Give the extent of all uninfected red blood cells.
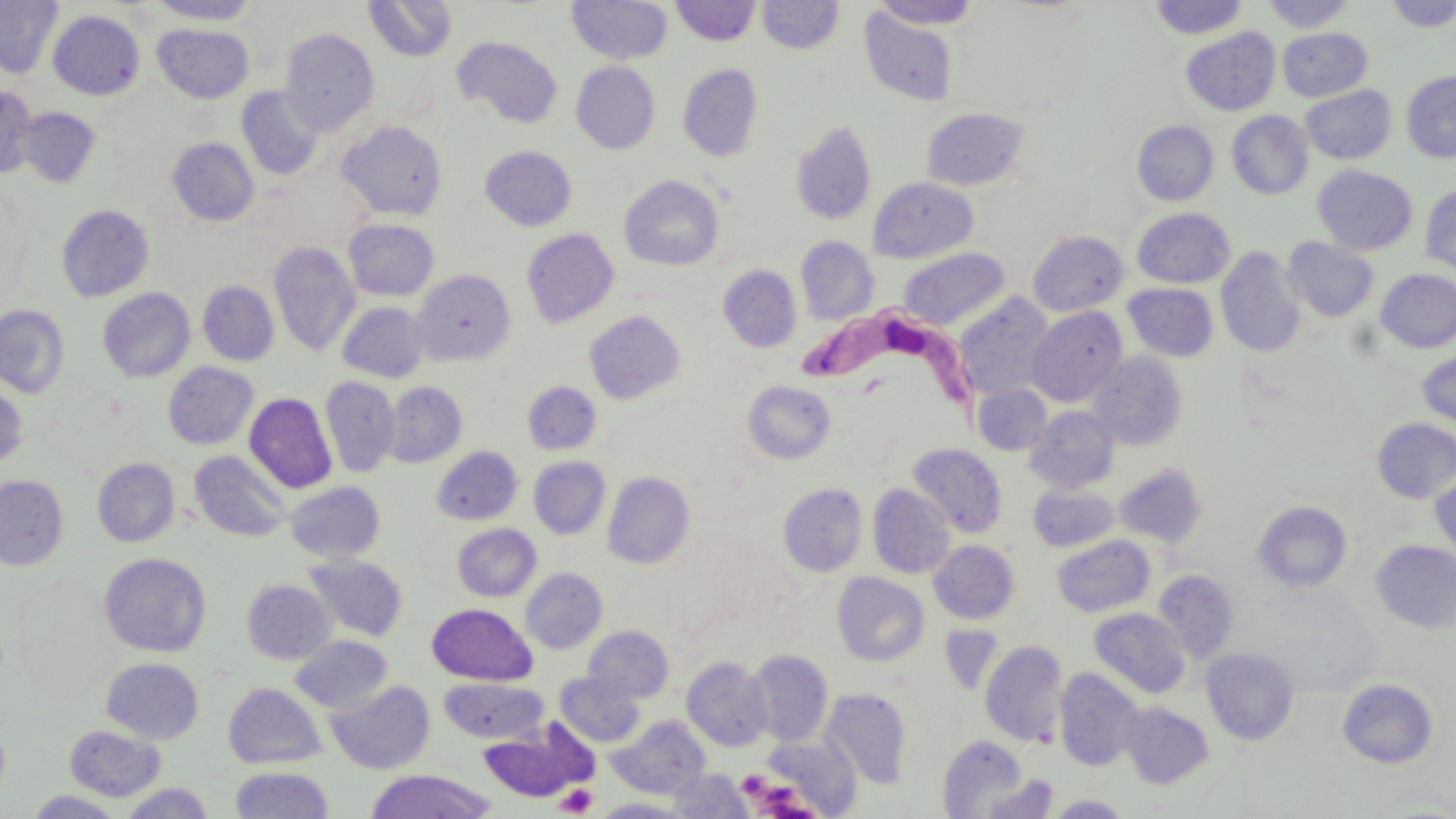
Approximate bounding boxes as (x1, y1, x2, y2) in pixels.
Uninfected red blood cells: (0, 0, 63, 78), (148, 0, 261, 24), (364, 0, 457, 61), (567, 0, 673, 65), (671, 0, 761, 46), (1148, 0, 1250, 39), (1261, 0, 1358, 32), (1383, 0, 1455, 32), (757, 1, 844, 54), (869, 1, 983, 29), (858, 6, 962, 107), (48, 10, 145, 100), (153, 23, 253, 103), (1180, 26, 1281, 116), (1277, 27, 1373, 102), (280, 28, 379, 135), (453, 36, 563, 128), (571, 62, 661, 154), (678, 64, 763, 161), (1402, 71, 1456, 163), (1300, 85, 1396, 164), (0, 86, 40, 180), (236, 86, 325, 180), (16, 107, 101, 188), (920, 107, 1031, 192), (1227, 110, 1314, 199), (337, 120, 447, 221), (790, 120, 877, 225), (1132, 120, 1219, 206), (167, 137, 259, 226), (480, 145, 577, 231), (1312, 164, 1417, 256), (620, 175, 725, 271), (869, 177, 979, 263), (1421, 185, 1456, 277), (55, 204, 155, 302), (1132, 208, 1235, 288), (343, 219, 439, 301), (522, 228, 620, 328), (1028, 230, 1129, 316), (796, 236, 878, 325), (1282, 237, 1379, 322), (268, 240, 361, 358), (898, 247, 1010, 330), (1216, 248, 1307, 357), (717, 265, 802, 352), (1376, 268, 1456, 353), (413, 269, 515, 366), (197, 281, 279, 366), (1123, 283, 1219, 362), (97, 288, 196, 383), (954, 294, 1055, 402), (337, 301, 430, 383), (0, 304, 70, 398), (1027, 305, 1127, 407), (584, 310, 686, 405), (1416, 348, 1456, 429), (1088, 351, 1189, 451), (163, 362, 259, 450), (320, 376, 401, 477), (742, 380, 837, 465), (383, 381, 467, 468), (522, 381, 601, 455), (0, 382, 29, 469), (973, 384, 1052, 456), (244, 392, 337, 493), (1025, 406, 1119, 493), (1373, 418, 1456, 503), (907, 442, 1007, 538), (431, 446, 523, 525), (189, 450, 291, 543), (529, 456, 610, 539), (92, 457, 180, 547), (1113, 463, 1208, 548), (1430, 471, 1456, 561), (602, 472, 694, 569), (0, 474, 69, 570), (285, 481, 385, 563), (778, 482, 868, 577), (868, 484, 956, 579), (1028, 484, 1120, 552), (1254, 500, 1353, 592), (452, 523, 541, 602), (1051, 535, 1155, 617), (929, 540, 1020, 624), (1371, 540, 1456, 633), (99, 552, 211, 657), (303, 555, 407, 641), (520, 567, 607, 654), (1153, 570, 1239, 662), (832, 572, 930, 667), (242, 579, 335, 664), (427, 603, 537, 685), (1089, 608, 1191, 699), (583, 625, 674, 704), (938, 625, 1004, 695), (290, 635, 393, 713), (980, 640, 1068, 747), (1201, 647, 1299, 745), (746, 649, 833, 746), (681, 657, 773, 752), (101, 658, 203, 744), (1054, 669, 1144, 771), (554, 673, 645, 747), (439, 678, 547, 743), (1337, 678, 1438, 768), (326, 680, 435, 775), (223, 682, 326, 769), (821, 688, 911, 789), (1120, 702, 1214, 789), (607, 716, 710, 799), (477, 720, 596, 804), (65, 724, 167, 801), (762, 733, 862, 816), (937, 735, 1033, 818), (230, 766, 334, 819), (364, 769, 495, 818), (667, 769, 752, 817), (977, 775, 1060, 819), (120, 783, 215, 818), (24, 790, 125, 818), (1048, 794, 1131, 817), (595, 798, 688, 818).

Trypanosoma brucei locations: (786, 301, 988, 414). Platelet locations: (737, 770, 770, 797), (763, 782, 804, 816), (555, 784, 597, 816). Slide-level diagnosis: Trypanosoma brucei. Light microscopy. Image is 1456×819 pixels. Single field of view. May-Grünwald-Giemsa-stained preparation. Captured at 1000x magnification. Thin blood film.